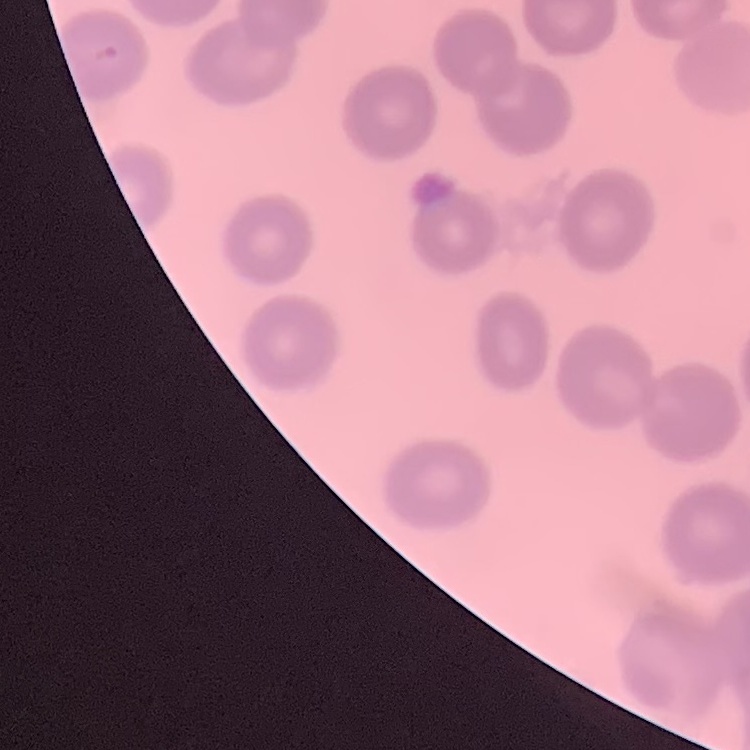
red blood cell morphology = no rouleaux formation
stain = Field's or Giemsa
image type = square crop of a larger photomicrograph
preparation = thin blood film